Locate platelets.
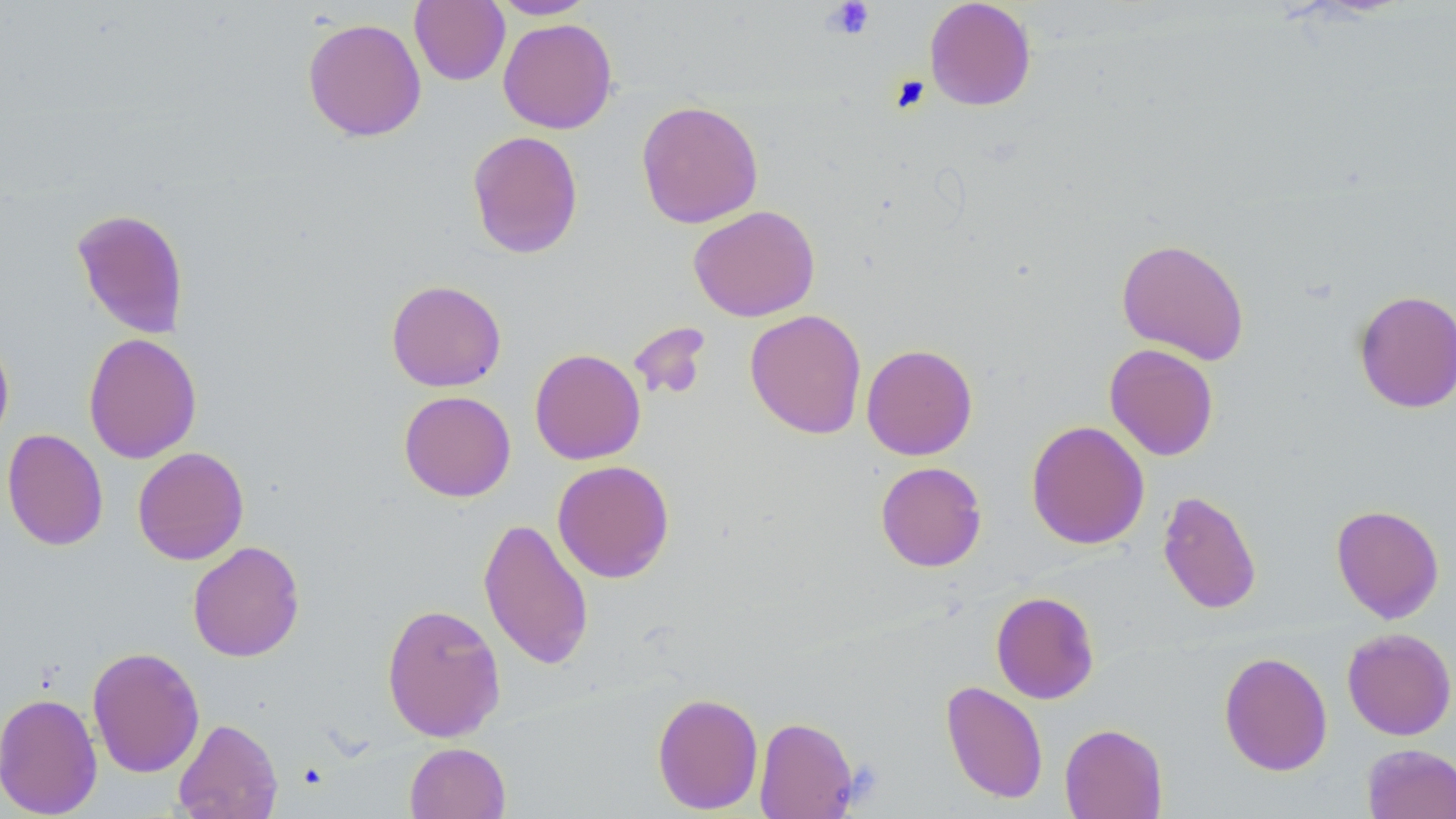
Approximate bounding boxes as (x1, y1, x2, y2) in pixels.
Platelets: (821, 1, 875, 40).

Uninfected red blood cell locations: (410, 0, 510, 86), (489, 0, 596, 19), (924, 0, 1037, 111), (302, 17, 427, 142), (498, 18, 618, 134), (636, 100, 764, 228), (466, 130, 584, 259), (689, 205, 820, 322), (72, 208, 190, 338), (1116, 237, 1250, 364), (386, 279, 507, 392), (1353, 288, 1456, 413), (745, 309, 867, 439), (629, 322, 712, 403), (0, 332, 14, 450), (83, 332, 201, 464), (861, 343, 978, 460), (1104, 344, 1219, 461), (529, 348, 646, 464), (398, 390, 516, 502), (1026, 420, 1149, 550), (2, 428, 108, 551), (132, 446, 249, 565), (552, 460, 674, 583), (875, 461, 987, 571), (1157, 490, 1262, 615), (1331, 503, 1445, 623), (478, 516, 594, 671), (187, 541, 305, 662), (990, 591, 1100, 704), (381, 602, 506, 742), (1342, 627, 1456, 740), (87, 646, 205, 778), (1218, 651, 1333, 776), (940, 680, 1048, 804), (0, 691, 103, 818), (652, 692, 764, 814), (754, 716, 858, 818), (172, 717, 283, 819), (1059, 723, 1168, 818), (404, 742, 510, 819), (1360, 743, 1456, 819). Slide-level diagnosis: no evidence of blood parasites. Thin blood smear. Optical microscopy. Image is 1456×819 pixels. 1000x magnification. One field of a larger specimen. May-Grünwald-Giemsa stain.